Assess this cell for malaria.
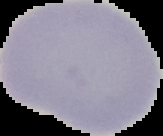
It is uninfected.

Summary:
  - Image type: cell region segmented out of the field of view; surrounding area masked to black
  - Preparation: thin blood smear
  - Image size: 163×136 pixels